Identify the blood parasite species.
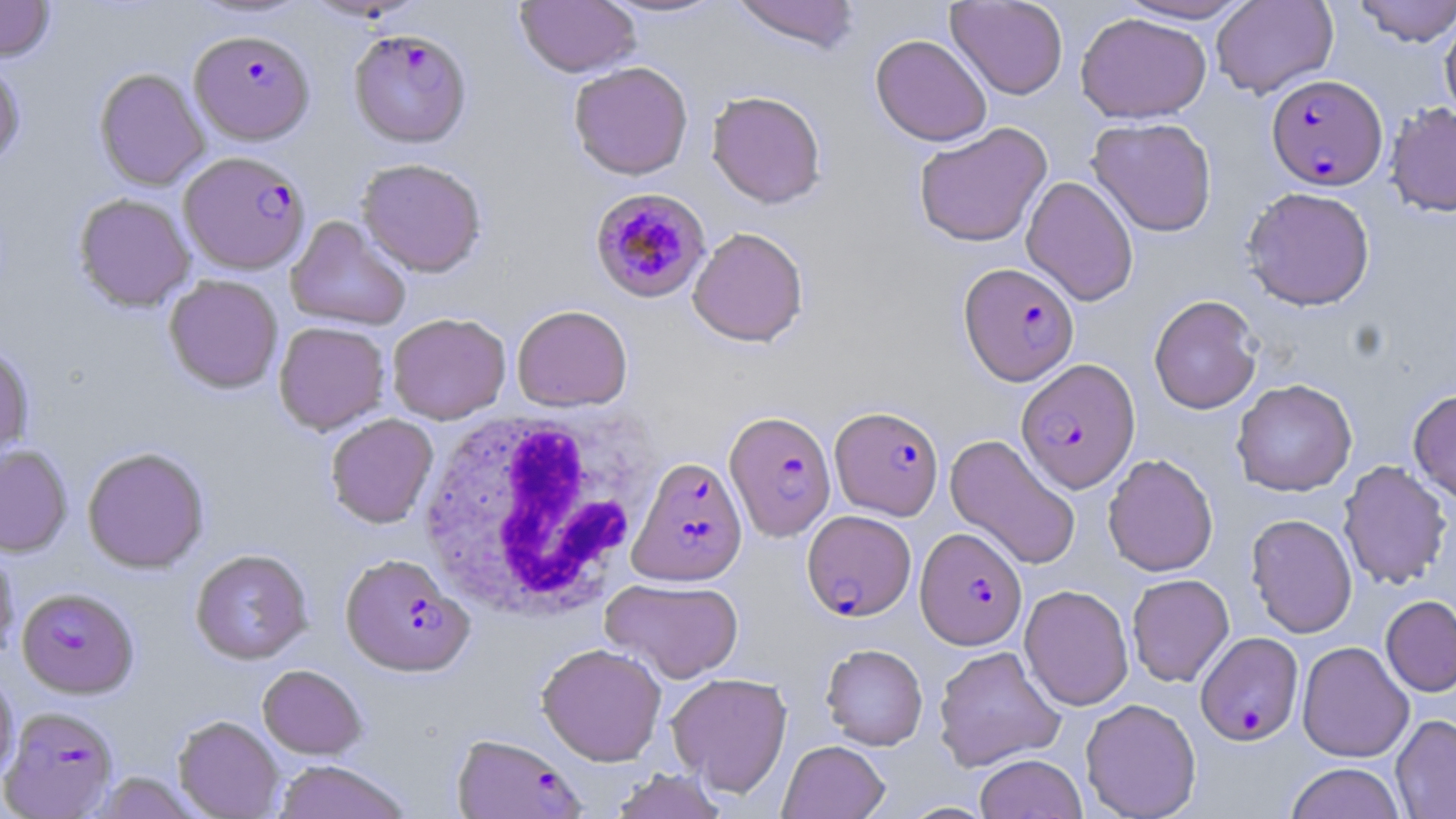
Plasmodium falciparum.

Approximate bounding boxes as [x1, y1, x2, y2] in pixels. Plasmodium falciparum-infected red blood cell locations: [348, 28, 472, 148], [189, 29, 314, 145], [1266, 74, 1387, 190], [179, 151, 311, 275], [589, 187, 711, 304], [958, 262, 1079, 386], [1016, 358, 1140, 493], [829, 406, 944, 520], [724, 410, 837, 541], [629, 457, 748, 586], [802, 510, 916, 621], [915, 526, 1027, 649], [340, 553, 474, 678], [17, 587, 139, 699], [1196, 631, 1304, 745], [0, 706, 119, 819], [451, 733, 584, 818]. White blood cell locations: [419, 406, 655, 621]. Uninfected red blood cell locations: [0, 0, 55, 62], [188, 0, 313, 21], [598, 0, 729, 18], [730, 0, 861, 53], [946, 0, 1068, 100], [1113, 0, 1259, 24], [1211, 0, 1338, 99], [1353, 0, 1455, 46], [515, 1, 641, 78], [1075, 12, 1211, 123], [1440, 16, 1456, 122], [870, 33, 992, 146], [0, 58, 26, 170], [568, 61, 693, 180], [94, 67, 209, 190], [706, 89, 827, 208], [1385, 102, 1456, 216], [1086, 117, 1218, 236], [913, 122, 1052, 248], [356, 157, 487, 277], [1021, 175, 1139, 306], [1241, 186, 1376, 311], [73, 193, 195, 312], [285, 215, 411, 332], [688, 226, 809, 346], [164, 274, 283, 394], [1149, 295, 1262, 414], [512, 305, 633, 412], [387, 312, 511, 424], [273, 321, 390, 435], [0, 343, 34, 463], [1231, 379, 1358, 496], [1408, 388, 1456, 504], [325, 414, 438, 528], [944, 433, 1082, 571], [0, 445, 72, 557], [82, 446, 209, 574], [1103, 453, 1218, 577], [1337, 460, 1452, 590], [1246, 513, 1358, 638], [0, 540, 19, 663], [190, 549, 312, 665], [1127, 573, 1234, 687], [601, 578, 743, 683], [1020, 584, 1133, 711], [1381, 594, 1456, 697], [1297, 641, 1414, 762], [537, 642, 666, 766], [821, 643, 928, 750], [932, 645, 1066, 772], [257, 665, 367, 760], [0, 669, 19, 785], [666, 672, 793, 797], [1080, 698, 1201, 819], [1391, 714, 1456, 819], [173, 716, 284, 818], [778, 740, 889, 819], [975, 753, 1087, 819], [272, 760, 412, 819], [1285, 762, 1405, 819], [608, 769, 729, 819], [91, 772, 200, 818]. Image is 1456×819 pixels. May-Grünwald-Giemsa-stained preparation. 1000x magnification. Thin blood film. Optical microscopy. Single field of view.